Name the parasite shown.
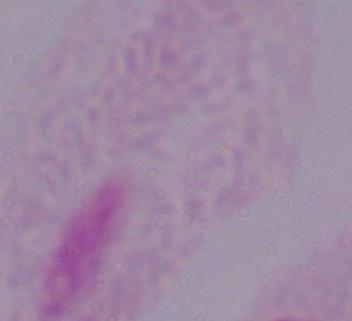

This is a trichomonad.

Summary:
  - Modality: micrograph
  - Magnification: 1000x